Locate leukocytes (white blood cells).
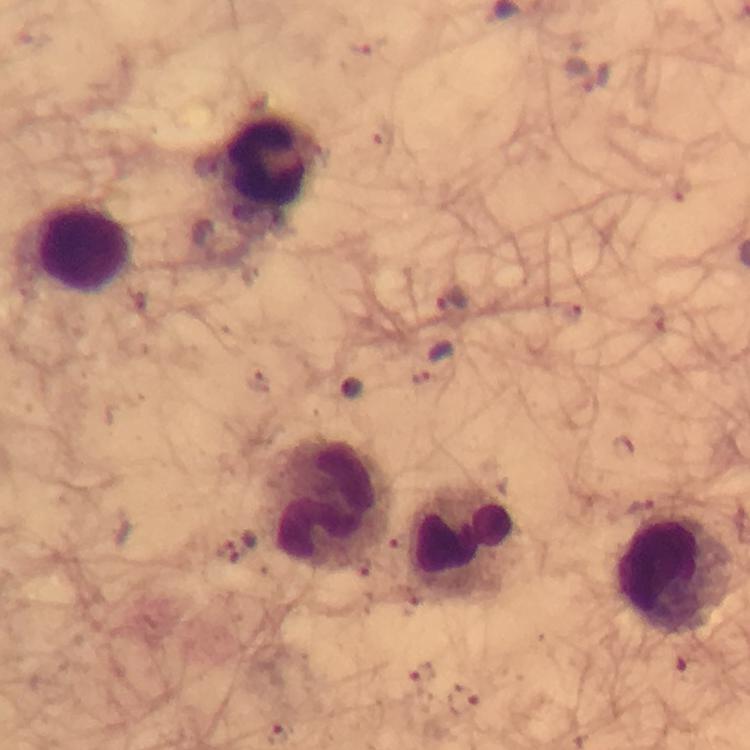

Approximate centers as [x, y] in pixels.
Leukocytes: [268, 161], [84, 243], [326, 504], [467, 545], [675, 577].

preparation = thick blood film
context = from a malaria diagnostic workup
malaria parasite locations = approximate centers as [x, y] in pixels: [365, 46], [580, 74], [451, 301], [432, 361], [259, 381], [690, 669], [421, 674], [462, 699]
magnification = 100x
capture = smartphone photograph through a microscope
cropped from = a single field of view
image size = 750×750 pixels
stain = Giemsa
immersion oil = used